Classify this cell by malaria status.
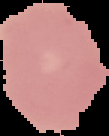
It is uninfected.

image type = segmented cell region on a black background
preparation = thin blood film
image size = 109×136 pixels